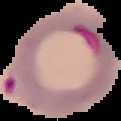
Summary:
  - Image size: 121×121 pixels
  - Malaria status: parasitized
  - Preparation: thin blood smear
  - Image type: cell region segmented out of the field of view; surrounding area masked to black